Report the malaria status of this cell.
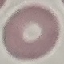

Uninfected.

image_type: cell patch, automatically extracted from a larger field of view and resized to 64 × 64 pixels
stain: Giemsa
preparation: thin smear
capture: smartphone camera at the microscope eyepiece